Assess the morphology of the erythrocytes.
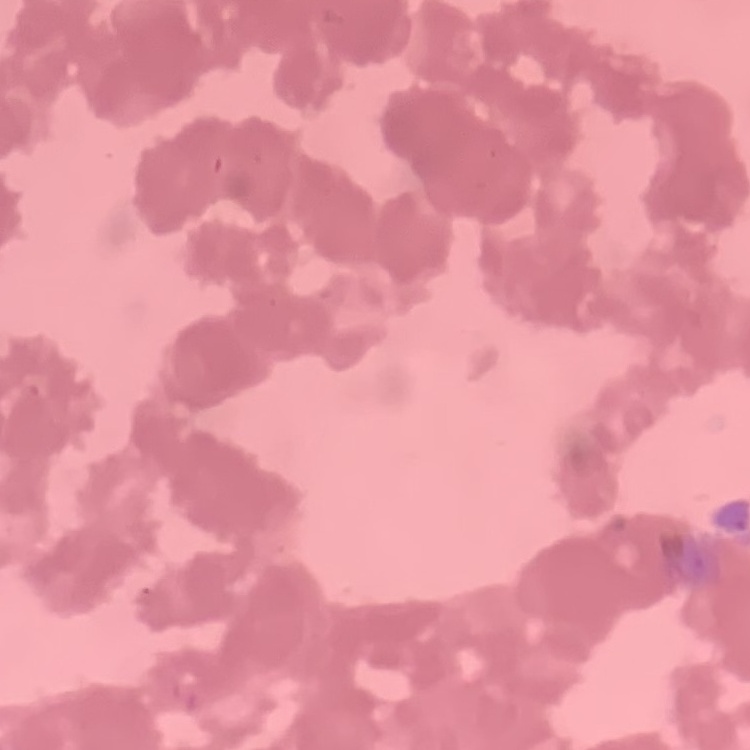

They show rouleaux formation.

Summary:
  - Image type: one tile cut from a larger photomicrograph
  - Stain: Field's or Giemsa
  - Preparation: thin peripheral smear